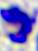

Micrograph. A white blood cell is seen. Captured at 400x magnification.